Give the preparation type.
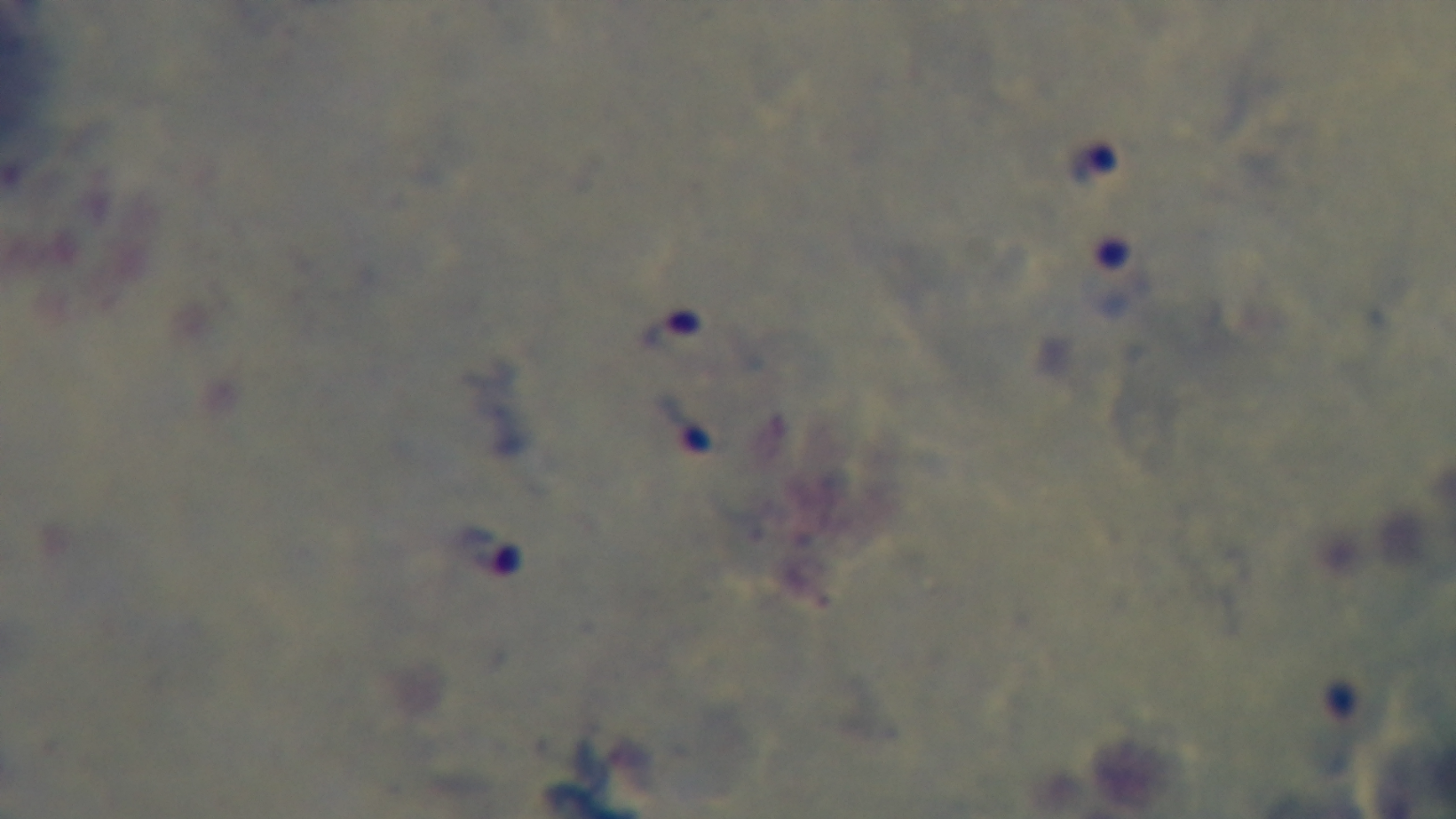

It is a thick blood film.

Oil-immersion objective, 100x. Mounted 4K digital camera. Malaria status: positive. Light microscopy. One field from the slide. Giemsa stain.